Name the cell type shown.
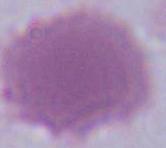
An erythrocyte.

{
  "magnification": "1000x",
  "modality": "photomicrograph"
}